Name the parasite shown.
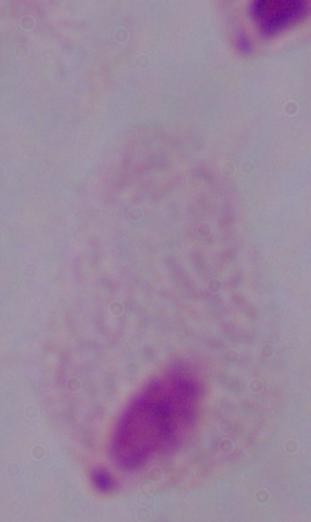
This is a trichomonad.

Captured at 1000x magnification. Micrograph.